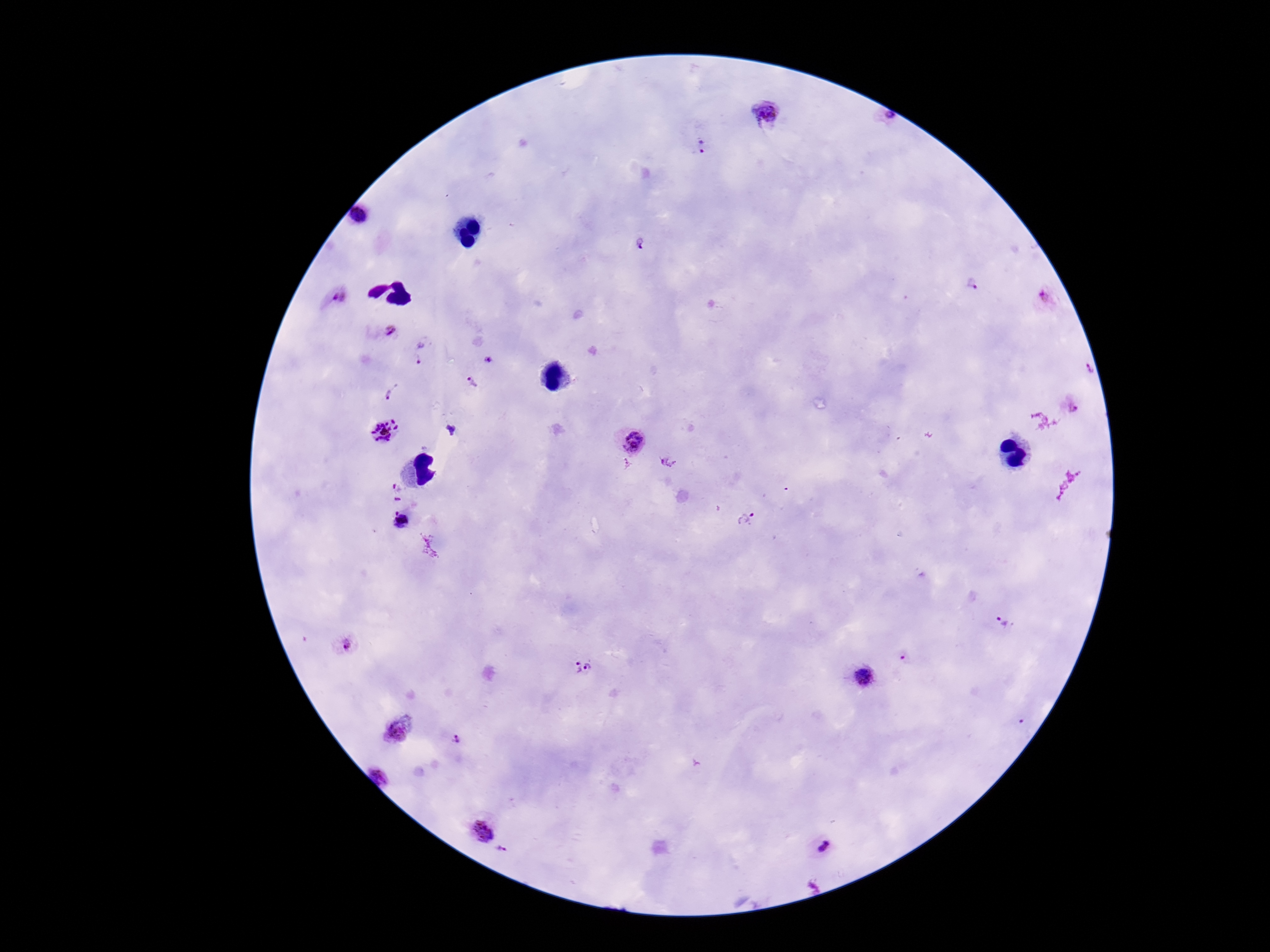
Approximate object centers, in pixels from the top-left corner. Plasmodium parasite locations: (x=765, y=114), (x=883, y=118), (x=702, y=146), (x=360, y=214), (x=640, y=243), (x=973, y=285), (x=340, y=297), (x=1044, y=297), (x=391, y=330), (x=420, y=350), (x=487, y=359), (x=1087, y=371), (x=473, y=383), (x=392, y=390), (x=1071, y=407), (x=385, y=431), (x=629, y=439), (x=667, y=460), (x=396, y=486), (x=747, y=518), (x=1004, y=623), (x=346, y=645), (x=903, y=656), (x=590, y=667), (x=576, y=668), (x=864, y=678), (x=1023, y=724), (x=399, y=730), (x=455, y=740), (x=381, y=775), (x=483, y=830), (x=821, y=847), (x=503, y=851). Photographed through the microscope eyepiece with a smartphone camera. Giemsa stain. Image is 1270×952 pixels. Thick blood film. 100x magnification. Patient malaria status: positive. One field from this slide.